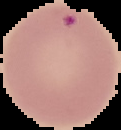
Summary:
  - Image size: 121×130 pixels
  - Malaria status: parasitized
  - Image type: segmented cell region on a black background
  - Preparation: thin blood film